Report the malaria status of this cell.
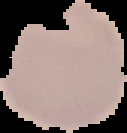

It is uninfected.

image type = segmented cell region with the area outside set to black
preparation = thin blood film
image size = 127×133 pixels